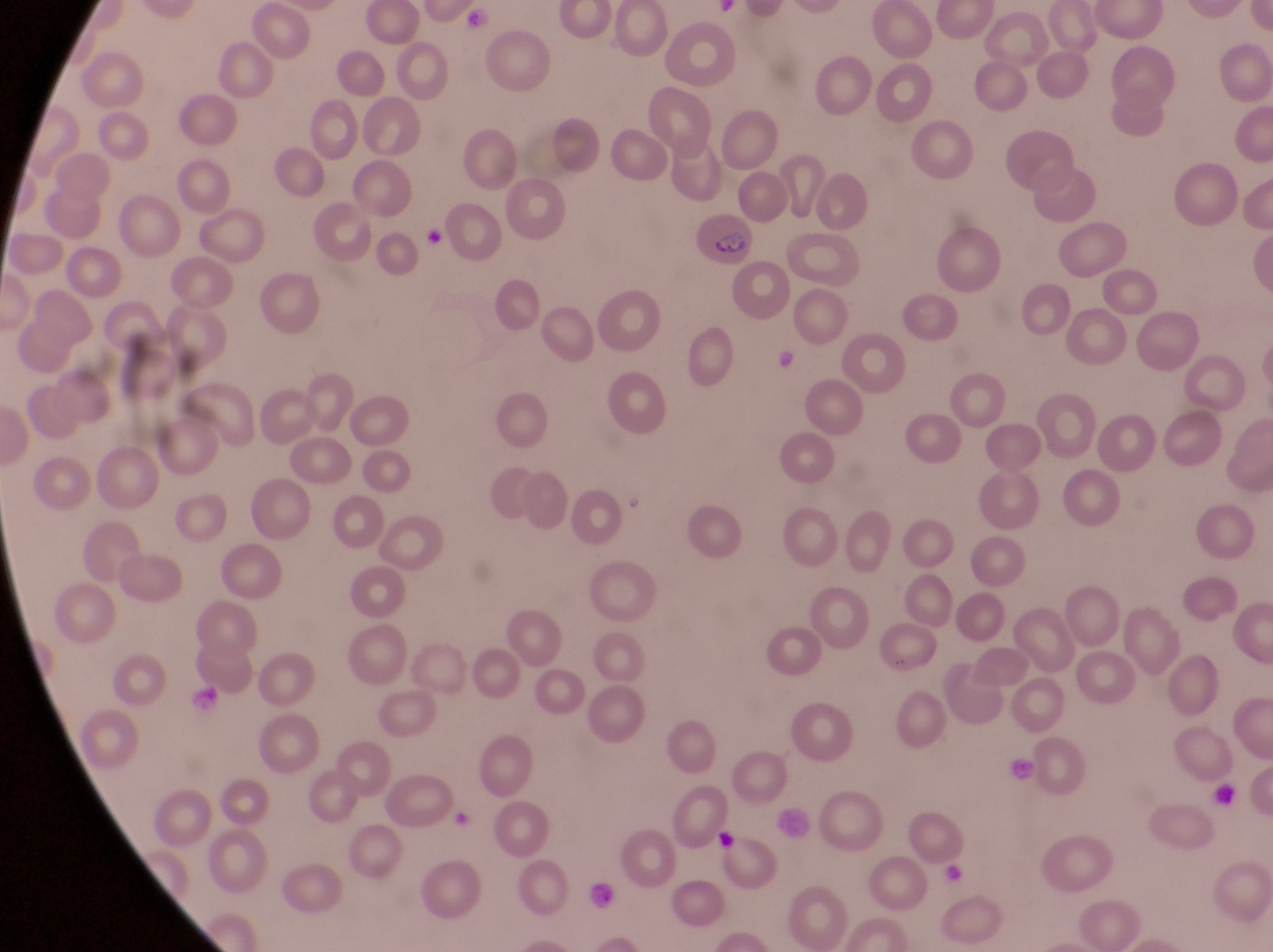
capture = smartphone photograph through the eyepiece of an Olympus CX-23 microscope
magnification = 1000x
image size = 1273×952 pixels
field of view = single
artifact (platelet-like body, stain precipitate, or debris) locations = approximate bounding boxes as [left, top, right, bottom] in pixels: [764, 342, 797, 374], [192, 686, 227, 721], [1003, 746, 1038, 788], [1211, 786, 1238, 808], [776, 802, 816, 842], [709, 826, 736, 856], [586, 874, 619, 914]
parasitised red blood cell locations = approximate bounding boxes as [left, top, right, bottom] in pixels: [694, 207, 757, 270]
country = Uganda
preparation = thin blood film